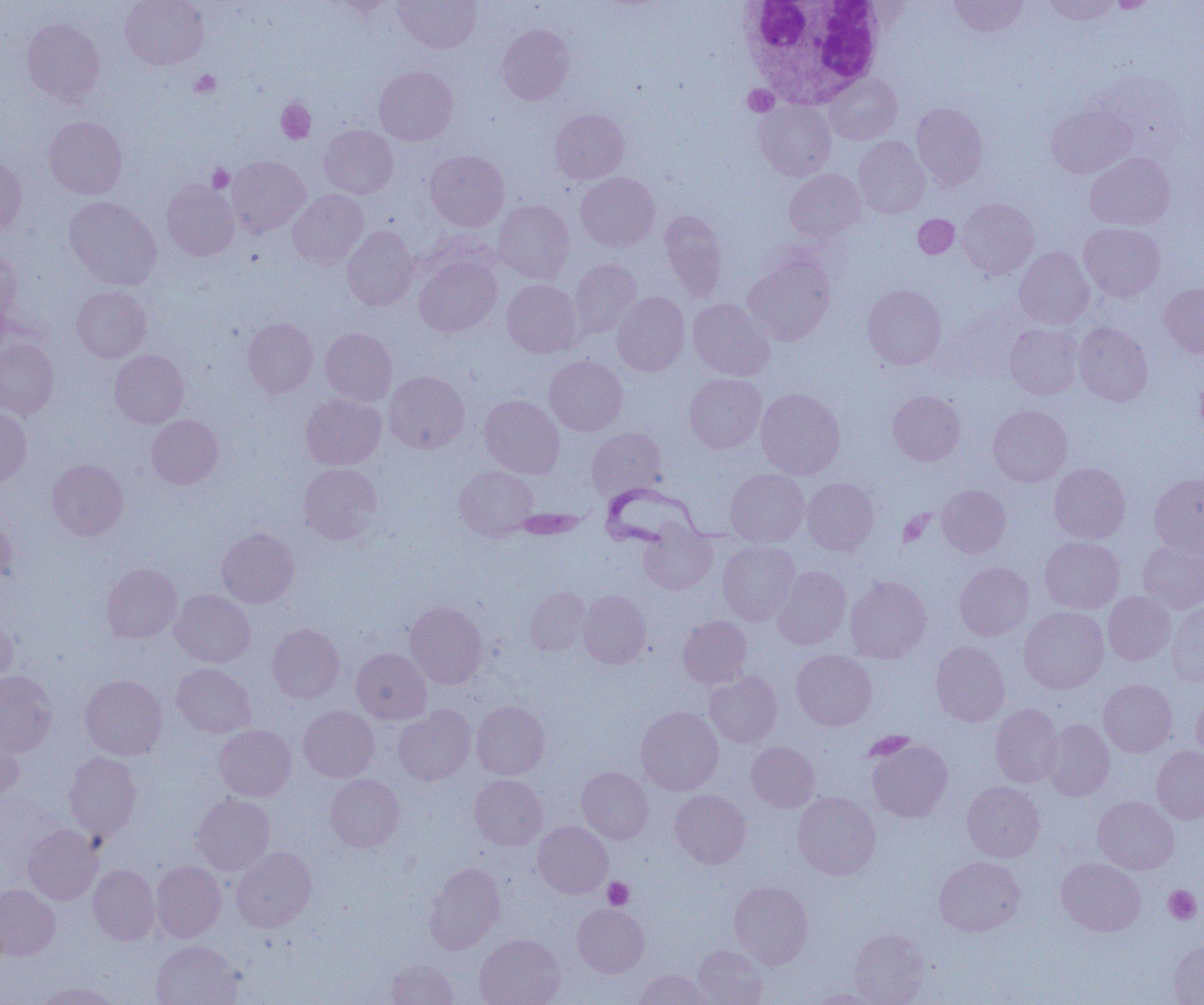

slide_level_diagnosis: Trypanosoma brucei
platelet_locations: 'approximate bounding boxes as named x1/y1/x2/y2 corners in pixels: (x1=190, y1=70, x2=221, y2=97), (x1=743, y1=85, x2=778, y2=116), (x1=277, y1=100, x2=316, y2=144), (x1=207, y1=164, x2=233, y2=192), (x1=898, y1=511, x2=933, y2=546), (x1=603, y1=877, x2=633, y2=909), (x1=1163, y1=885, x2=1201, y2=925)'
uninfected_red_blood_cell_locations: 'approximate bounding boxes as named x1/y1/x2/y2 corners in pixels: (x1=120, y1=0, x2=209, y2=69), (x1=394, y1=0, x2=482, y2=53), (x1=948, y1=0, x2=1029, y2=36), (x1=1040, y1=0, x2=1121, y2=26), (x1=1105, y1=0, x2=1160, y2=12), (x1=327, y1=1, x2=397, y2=18), (x1=22, y1=17, x2=105, y2=105), (x1=496, y1=24, x2=574, y2=105), (x1=374, y1=66, x2=458, y2=145), (x1=1090, y1=70, x2=1189, y2=156), (x1=824, y1=73, x2=902, y2=144), (x1=754, y1=98, x2=836, y2=180), (x1=1046, y1=102, x2=1135, y2=178), (x1=911, y1=103, x2=988, y2=190), (x1=550, y1=109, x2=629, y2=184), (x1=44, y1=116, x2=128, y2=199), (x1=319, y1=125, x2=398, y2=198), (x1=852, y1=136, x2=930, y2=218), (x1=425, y1=150, x2=509, y2=231), (x1=1085, y1=153, x2=1175, y2=231), (x1=227, y1=155, x2=310, y2=238), (x1=0, y1=156, x2=27, y2=235), (x1=785, y1=169, x2=865, y2=242), (x1=576, y1=172, x2=660, y2=252), (x1=162, y1=179, x2=240, y2=260), (x1=288, y1=190, x2=368, y2=268), (x1=64, y1=196, x2=161, y2=291), (x1=958, y1=198, x2=1039, y2=279), (x1=492, y1=200, x2=574, y2=283), (x1=660, y1=210, x2=728, y2=300), (x1=913, y1=215, x2=959, y2=258), (x1=1079, y1=222, x2=1165, y2=302), (x1=342, y1=226, x2=419, y2=310), (x1=1014, y1=247, x2=1094, y2=329), (x1=0, y1=248, x2=22, y2=325), (x1=743, y1=248, x2=836, y2=344), (x1=414, y1=255, x2=501, y2=337), (x1=569, y1=258, x2=643, y2=339), (x1=502, y1=279, x2=582, y2=358), (x1=1160, y1=283, x2=1204, y2=357), (x1=862, y1=284, x2=946, y2=369), (x1=71, y1=285, x2=151, y2=362), (x1=612, y1=292, x2=690, y2=376), (x1=688, y1=298, x2=773, y2=380), (x1=242, y1=318, x2=318, y2=397), (x1=1074, y1=321, x2=1153, y2=406), (x1=1005, y1=323, x2=1084, y2=400), (x1=320, y1=329, x2=397, y2=405), (x1=0, y1=338, x2=59, y2=418), (x1=109, y1=350, x2=189, y2=428), (x1=544, y1=355, x2=627, y2=436), (x1=384, y1=371, x2=469, y2=453), (x1=684, y1=374, x2=766, y2=453), (x1=756, y1=388, x2=845, y2=479), (x1=888, y1=390, x2=965, y2=466), (x1=301, y1=394, x2=386, y2=469), (x1=479, y1=395, x2=565, y2=478), (x1=988, y1=405, x2=1072, y2=487), (x1=0, y1=409, x2=31, y2=489), (x1=147, y1=414, x2=223, y2=489), (x1=586, y1=427, x2=667, y2=502), (x1=47, y1=459, x2=128, y2=540), (x1=1049, y1=462, x2=1130, y2=543), (x1=299, y1=463, x2=382, y2=544), (x1=455, y1=466, x2=539, y2=540), (x1=725, y1=469, x2=809, y2=546), (x1=1149, y1=473, x2=1204, y2=556), (x1=802, y1=477, x2=879, y2=555), (x1=937, y1=484, x2=1011, y2=557), (x1=0, y1=515, x2=17, y2=587), (x1=639, y1=523, x2=717, y2=595), (x1=216, y1=527, x2=299, y2=608), (x1=1040, y1=537, x2=1125, y2=613), (x1=1137, y1=539, x2=1204, y2=615), (x1=718, y1=540, x2=801, y2=624), (x1=955, y1=562, x2=1034, y2=640), (x1=101, y1=563, x2=182, y2=644), (x1=771, y1=567, x2=852, y2=649), (x1=844, y1=575, x2=932, y2=663), (x1=524, y1=586, x2=591, y2=656), (x1=170, y1=589, x2=255, y2=667), (x1=578, y1=590, x2=652, y2=668), (x1=1103, y1=591, x2=1176, y2=665), (x1=405, y1=601, x2=487, y2=688), (x1=1167, y1=601, x2=1204, y2=687), (x1=1019, y1=606, x2=1108, y2=694), (x1=0, y1=614, x2=17, y2=688), (x1=678, y1=616, x2=752, y2=688), (x1=267, y1=623, x2=345, y2=703), (x1=931, y1=641, x2=1010, y2=726), (x1=351, y1=648, x2=431, y2=724), (x1=791, y1=650, x2=877, y2=730), (x1=171, y1=664, x2=255, y2=738), (x1=0, y1=670, x2=57, y2=756), (x1=704, y1=672, x2=782, y2=747), (x1=81, y1=674, x2=167, y2=760), (x1=1099, y1=679, x2=1177, y2=757), (x1=1191, y1=694, x2=1204, y2=762), (x1=472, y1=701, x2=550, y2=780), (x1=990, y1=703, x2=1064, y2=787), (x1=299, y1=706, x2=378, y2=782), (x1=394, y1=706, x2=476, y2=785), (x1=636, y1=707, x2=724, y2=795), (x1=1042, y1=719, x2=1115, y2=801), (x1=215, y1=724, x2=296, y2=801), (x1=0, y1=730, x2=23, y2=805), (x1=866, y1=737, x2=953, y2=822), (x1=746, y1=741, x2=820, y2=812), (x1=1151, y1=746, x2=1204, y2=823), (x1=64, y1=752, x2=142, y2=840), (x1=577, y1=766, x2=653, y2=844), (x1=325, y1=774, x2=404, y2=851), (x1=469, y1=775, x2=547, y2=850), (x1=961, y1=780, x2=1044, y2=862), (x1=670, y1=789, x2=750, y2=869), (x1=793, y1=792, x2=881, y2=879), (x1=191, y1=794, x2=275, y2=875), (x1=1092, y1=796, x2=1179, y2=874), (x1=533, y1=821, x2=612, y2=898), (x1=23, y1=824, x2=102, y2=904), (x1=231, y1=846, x2=317, y2=932), (x1=934, y1=856, x2=1025, y2=937), (x1=1057, y1=858, x2=1145, y2=936), (x1=152, y1=860, x2=226, y2=943), (x1=424, y1=862, x2=505, y2=954), (x1=88, y1=864, x2=159, y2=945), (x1=729, y1=880, x2=814, y2=969), (x1=0, y1=884, x2=60, y2=960), (x1=573, y1=903, x2=649, y2=977), (x1=849, y1=928, x2=930, y2=1005), (x1=474, y1=933, x2=565, y2=1005), (x1=1168, y1=939, x2=1204, y2=1004), (x1=151, y1=940, x2=242, y2=1005), (x1=693, y1=944, x2=768, y2=1005), (x1=386, y1=958, x2=459, y2=1005), (x1=634, y1=970, x2=713, y2=1004), (x1=35, y1=981, x2=120, y2=1005), (x1=808, y1=988, x2=887, y2=1004)'
preparation: thin blood smear
modality: optical microscopy
image_size: 1204×1005 pixels
trypanosoma_brucei_locations: 'approximate bounding boxes as named x1/y1/x2/y2 corners in pixels: (x1=594, y1=482, x2=723, y2=551)'
white_blood_cell_locations: 'approximate bounding boxes as named x1/y1/x2/y2 corners in pixels: (x1=737, y1=0, x2=886, y2=107)'
magnification: 1000x
field_of_view: one of a larger specimen